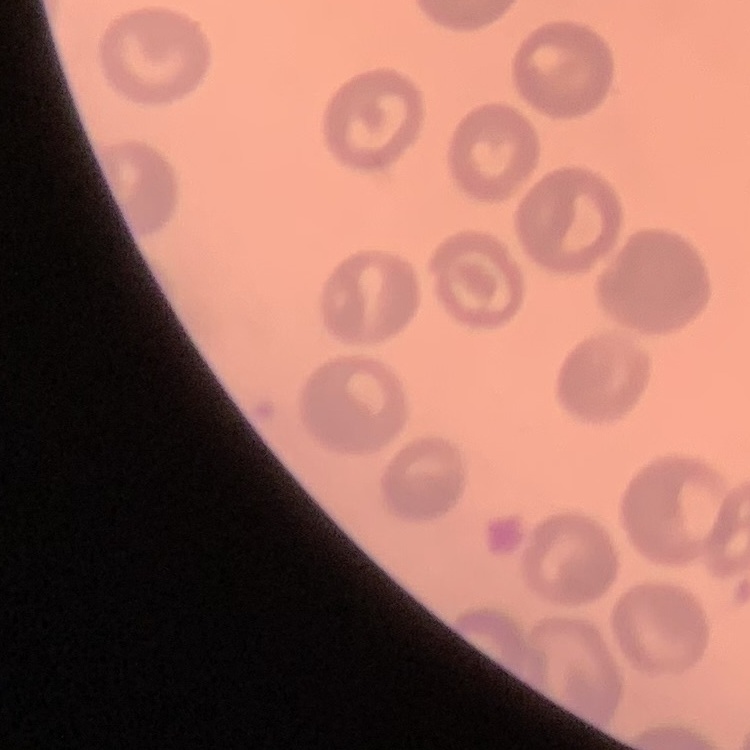

Summary:
  - Erythrocyte morphology: no rouleaux formation
  - Stain: Field's or Giemsa
  - Preparation: thin blood film
  - Image type: one tile cut from a larger photomicrograph